Classify this cell by malaria status.
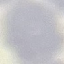
It is uninfected.

Summary:
  - Image type: automatically extracted cell patch, resized to 64 × 64 pixels
  - Preparation: thin blood smear
  - Stain: Giemsa
  - Capture: smartphone through the microscope eyepiece